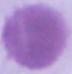
{
  "modality": "photomicrograph",
  "magnification": "1000x",
  "identification": "erythrocyte"
}